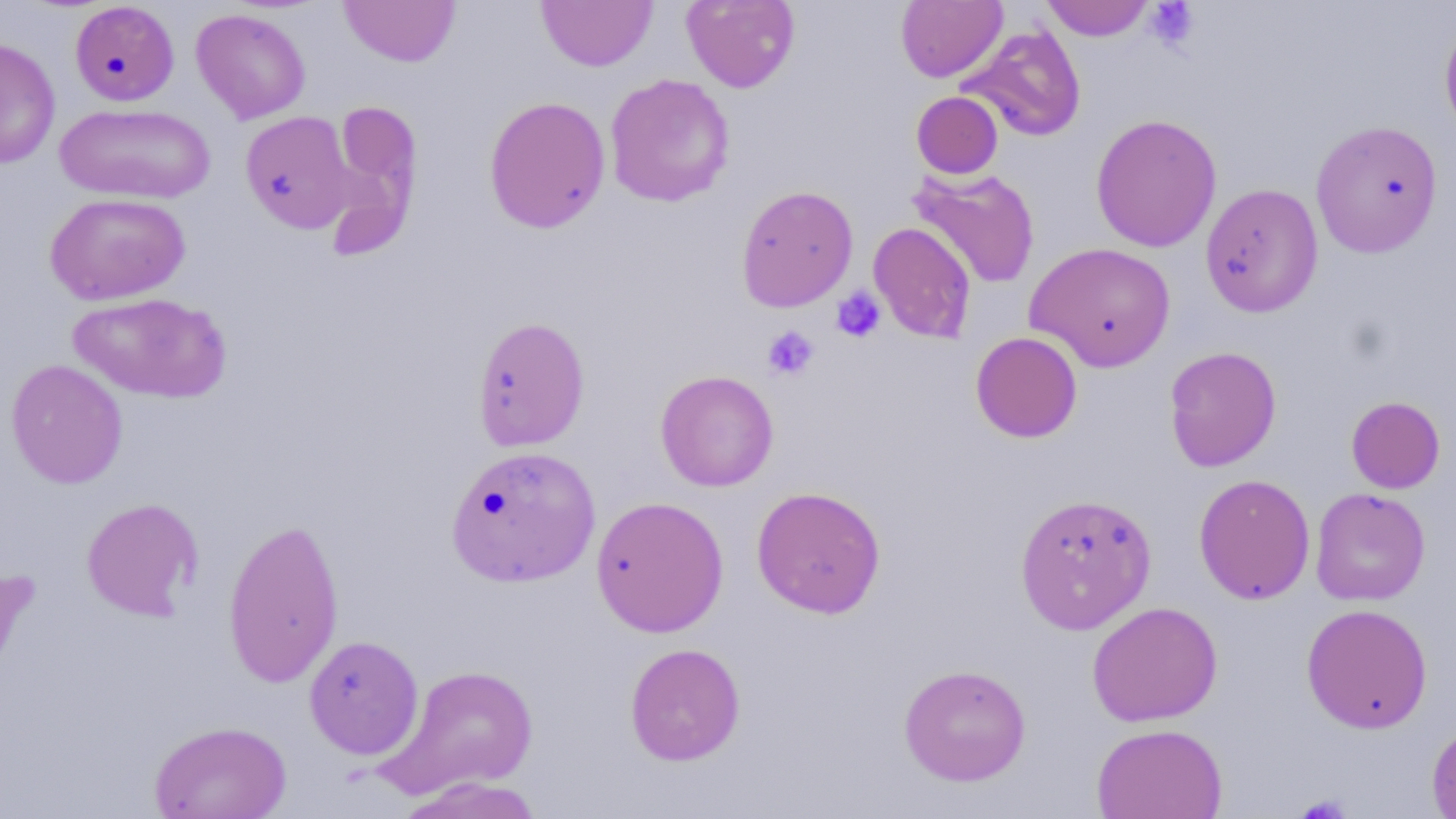

slide-level diagnosis = negative for blood parasites
platelet locations = approximate bounding boxes as [x1, y1, x2, y2] in pixels: [1144, 2, 1200, 49], [830, 286, 887, 343], [762, 326, 819, 381], [1296, 793, 1353, 819]
stain = May-Grünwald-Giemsa
uninfected red blood cell locations = approximate bounding boxes as [x1, y1, x2, y2] in pixels: [681, 0, 800, 93], [896, 0, 1007, 83], [1040, 0, 1156, 41], [70, 1, 179, 106], [338, 1, 460, 67], [537, 1, 657, 71], [191, 8, 311, 124], [1439, 14, 1456, 143], [960, 25, 1086, 143], [0, 37, 61, 169], [604, 73, 736, 208], [911, 91, 1003, 179], [483, 95, 611, 234], [322, 101, 424, 259], [54, 102, 215, 204], [240, 111, 358, 233], [1090, 113, 1222, 253], [1310, 119, 1444, 257], [908, 166, 1040, 290], [1199, 182, 1324, 318], [735, 185, 858, 312], [43, 192, 190, 306], [867, 222, 977, 344], [1025, 241, 1176, 372], [67, 292, 232, 403], [471, 316, 591, 451], [970, 331, 1083, 443], [1164, 346, 1282, 472], [5, 359, 128, 489], [655, 369, 779, 491], [1346, 396, 1446, 494], [453, 450, 599, 585], [1193, 473, 1315, 605], [750, 485, 886, 619], [1309, 487, 1431, 606], [1014, 492, 1157, 634], [590, 495, 729, 638], [81, 497, 203, 621], [222, 517, 345, 687], [0, 565, 37, 709], [1087, 601, 1223, 726], [1301, 603, 1433, 733], [303, 634, 424, 760], [625, 642, 745, 765], [898, 663, 1031, 786], [382, 664, 538, 797], [149, 719, 292, 819], [1426, 721, 1456, 819], [1091, 722, 1228, 819], [395, 776, 548, 818]
field of view = one of a larger specimen
magnification = 1000x
preparation = thin blood film
image size = 1456×819 pixels
modality = optical microscopy